Assess this cell for malaria.
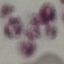
It is uninfected.

Summary:
  - Stain: Giemsa
  - Capture: smartphone through the microscope eyepiece
  - Image type: automatically extracted cell patch, resized to 64 × 64 pixels
  - Preparation: thin smear